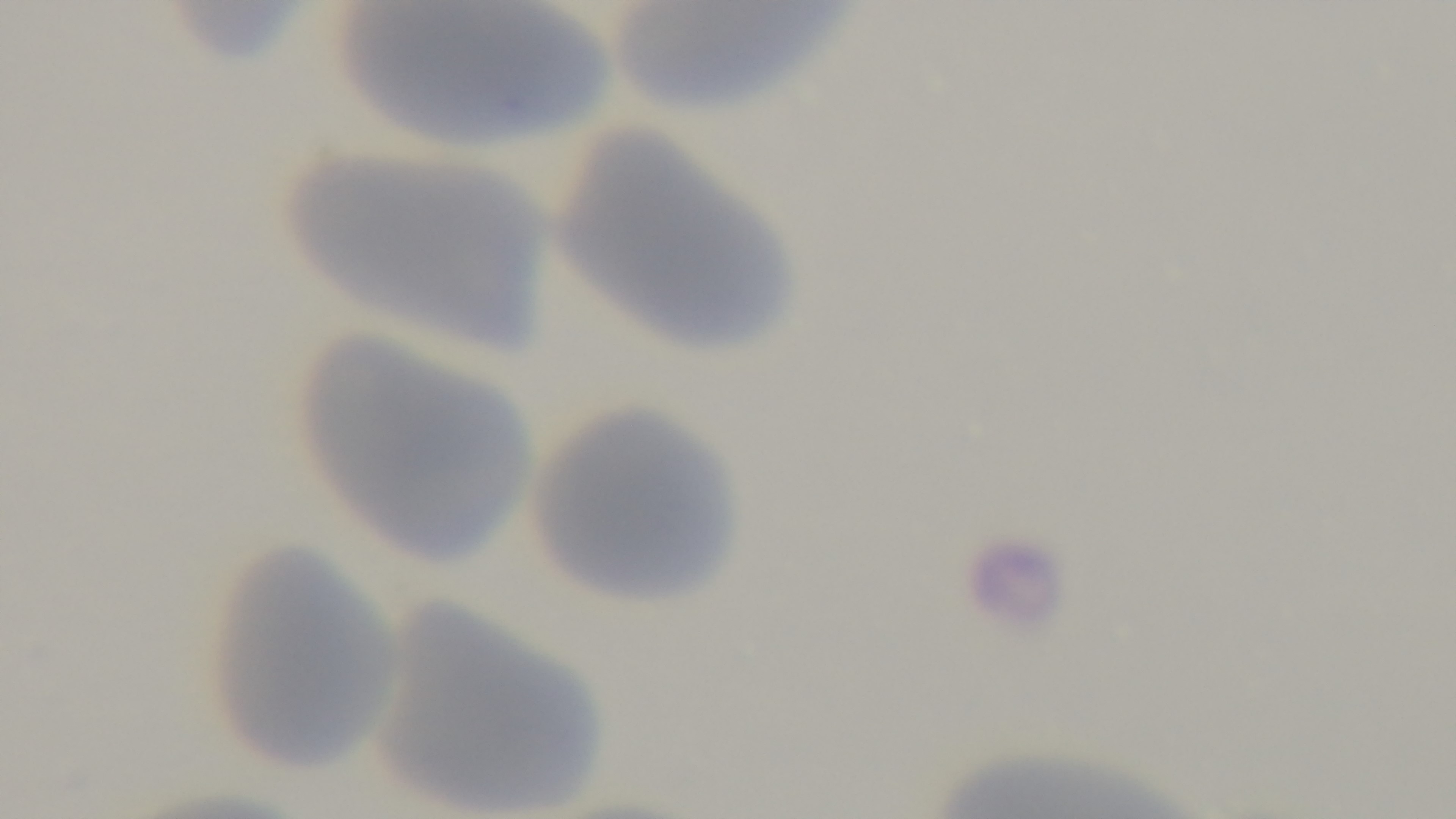
Summary:
  - Capture: mounted 4K digital camera
  - Preparation: thin smear
  - Modality: light microscopy
  - Stain: Giemsa
  - Objective: 100x oil immersion
  - Field of view: single
  - Malaria status: uninfected